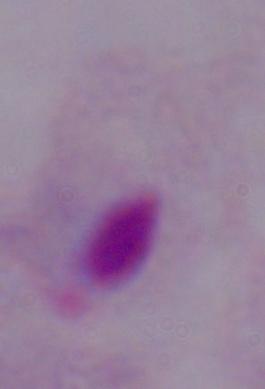 1000x magnification. A trichomonad is shown. Photomicrograph.